Report the malaria status of this cell.
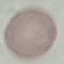
Uninfected.

Summary:
  - Capture: smartphone camera at the microscope eyepiece
  - Image type: automatically extracted cell patch, resized to 64 × 64 pixels
  - Preparation: thin blood film
  - Stain: Giemsa